State which cell type is depicted.
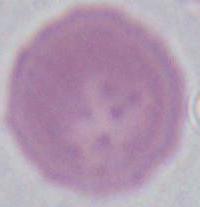

This is an erythrocyte.

magnification = 1000x
modality = micrograph